Identify the preparation type.
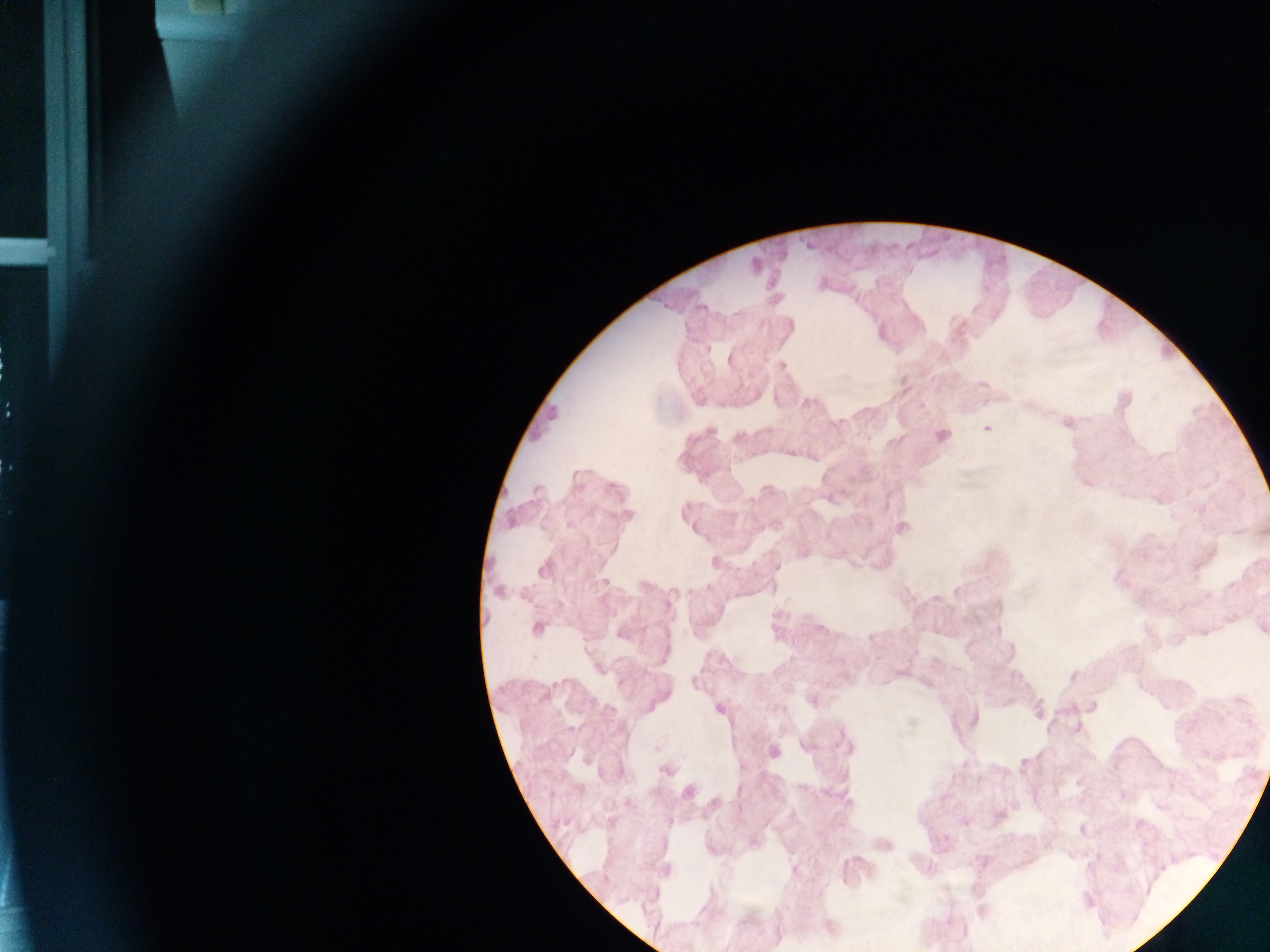

This is a thick smear.

Approximate centers as [x, y] in pixels.
Summary:
  - Plasmodium parasite locations: [730, 360], [782, 365], [1123, 400], [1067, 422], [987, 429], [941, 436], [627, 514], [687, 514], [902, 527], [714, 562], [543, 568], [499, 592], [537, 627], [1262, 627], [898, 672], [1072, 676], [812, 700], [719, 708], [1037, 710], [1076, 729], [848, 749], [772, 752], [665, 770], [687, 792], [715, 803], [998, 815], [964, 821], [1082, 830], [882, 843], [665, 870], [829, 927]
  - Country: Ghana
  - Field of view: single
  - Capture: mobile-phone photograph through a microscope
  - Image size: 1270×952 pixels